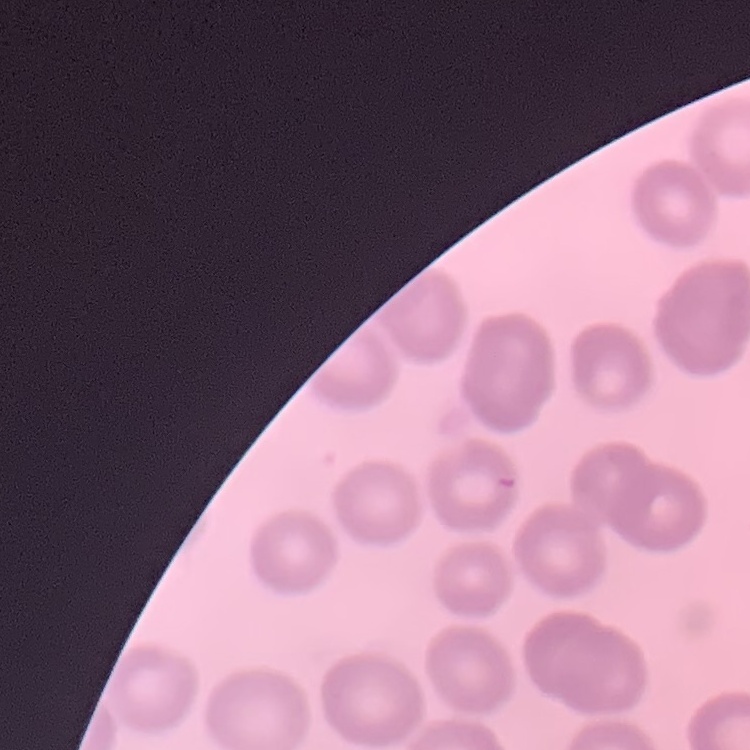

Summary:
  - Red blood cell morphology: no rouleaux formation
  - Stain: Field's or Giemsa
  - Image type: one tile cut from a larger photomicrograph
  - Preparation: thin blood smear